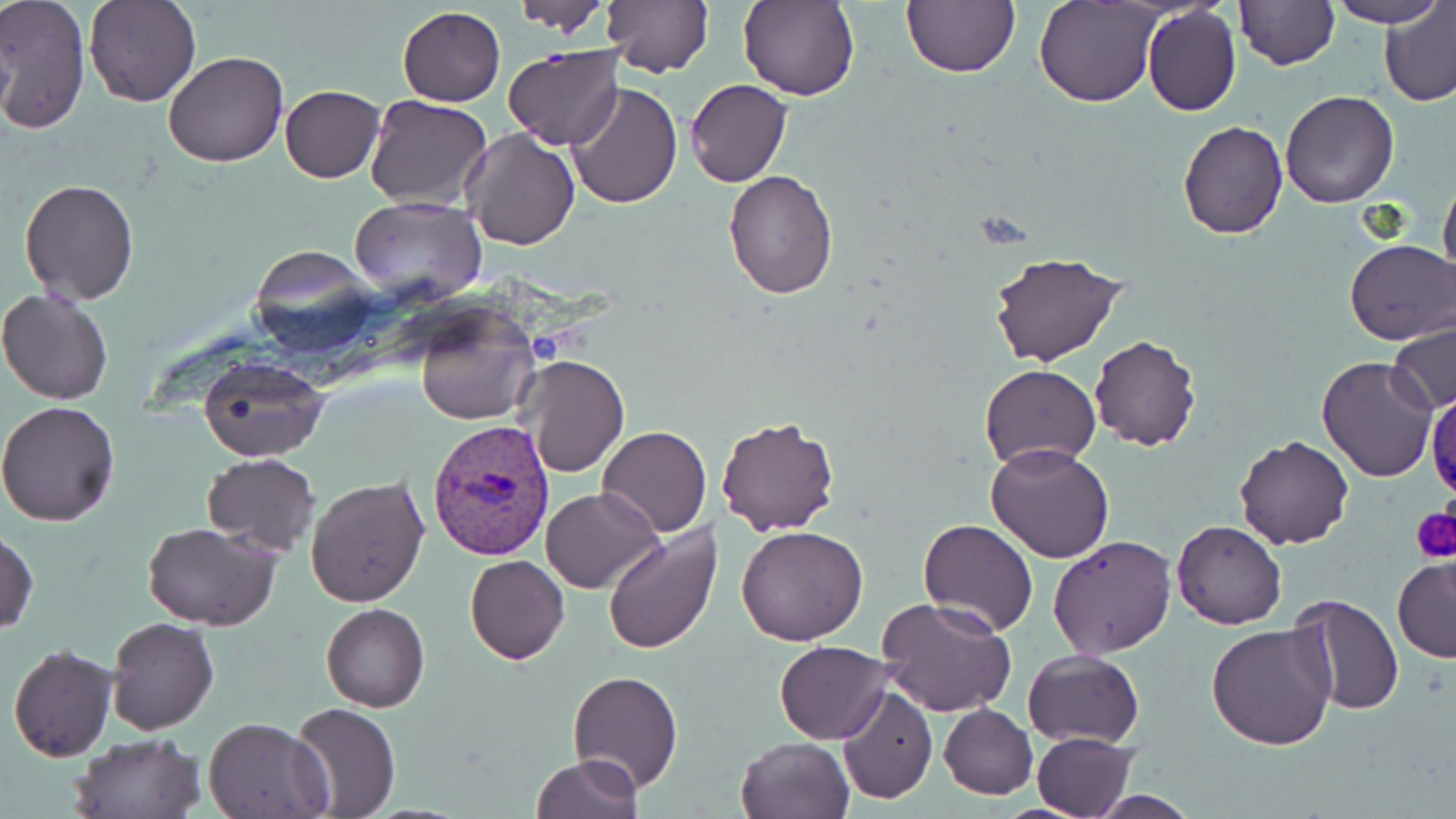
Approximate bounding boxes as named x1/y1/x2/y2 corners in pixels. Uninfected red blood cell locations: (x1=84, y1=0, x2=200, y2=106), (x1=603, y1=0, x2=713, y2=78), (x1=738, y1=0, x2=858, y2=101), (x1=901, y1=0, x2=1019, y2=78), (x1=1035, y1=0, x2=1161, y2=107), (x1=1326, y1=0, x2=1446, y2=26), (x1=1379, y1=0, x2=1456, y2=108), (x1=0, y1=1, x2=90, y2=133), (x1=507, y1=1, x2=609, y2=35), (x1=1233, y1=1, x2=1339, y2=70), (x1=1141, y1=5, x2=1242, y2=117), (x1=397, y1=7, x2=505, y2=105), (x1=504, y1=44, x2=624, y2=151), (x1=163, y1=51, x2=288, y2=167), (x1=685, y1=78, x2=792, y2=187), (x1=568, y1=81, x2=684, y2=211), (x1=279, y1=84, x2=384, y2=182), (x1=1280, y1=90, x2=1399, y2=209), (x1=363, y1=93, x2=492, y2=209), (x1=1177, y1=120, x2=1287, y2=239), (x1=461, y1=127, x2=581, y2=249), (x1=722, y1=169, x2=838, y2=300), (x1=1439, y1=176, x2=1456, y2=289), (x1=19, y1=177, x2=139, y2=303), (x1=348, y1=196, x2=487, y2=307), (x1=1345, y1=239, x2=1455, y2=346), (x1=987, y1=250, x2=1130, y2=369), (x1=0, y1=287, x2=116, y2=404), (x1=411, y1=300, x2=538, y2=425), (x1=1385, y1=318, x2=1454, y2=415), (x1=1088, y1=334, x2=1202, y2=452), (x1=520, y1=355, x2=628, y2=477), (x1=197, y1=356, x2=329, y2=461), (x1=1316, y1=356, x2=1439, y2=482), (x1=980, y1=364, x2=1102, y2=472), (x1=0, y1=400, x2=121, y2=527), (x1=715, y1=416, x2=839, y2=536), (x1=598, y1=425, x2=712, y2=538), (x1=1234, y1=435, x2=1355, y2=550), (x1=984, y1=443, x2=1115, y2=564), (x1=203, y1=453, x2=321, y2=556), (x1=305, y1=474, x2=430, y2=610), (x1=541, y1=487, x2=661, y2=594), (x1=917, y1=518, x2=1040, y2=638), (x1=1171, y1=519, x2=1287, y2=631), (x1=142, y1=521, x2=281, y2=631), (x1=602, y1=523, x2=723, y2=655), (x1=736, y1=525, x2=869, y2=646), (x1=1, y1=529, x2=38, y2=636), (x1=1047, y1=534, x2=1177, y2=658), (x1=465, y1=554, x2=568, y2=665), (x1=1392, y1=554, x2=1456, y2=664), (x1=1286, y1=594, x2=1402, y2=715), (x1=877, y1=597, x2=1017, y2=717), (x1=321, y1=603, x2=429, y2=712), (x1=106, y1=617, x2=219, y2=735), (x1=1205, y1=621, x2=1337, y2=751), (x1=774, y1=641, x2=892, y2=743), (x1=7, y1=643, x2=120, y2=763), (x1=1023, y1=647, x2=1144, y2=746), (x1=567, y1=670, x2=683, y2=792), (x1=835, y1=683, x2=938, y2=805), (x1=289, y1=701, x2=401, y2=817), (x1=939, y1=703, x2=1038, y2=798), (x1=204, y1=717, x2=329, y2=818), (x1=1030, y1=731, x2=1137, y2=819), (x1=68, y1=733, x2=202, y2=818), (x1=735, y1=736, x2=854, y2=819), (x1=531, y1=755, x2=643, y2=819). Platelet locations: (x1=1410, y1=504, x2=1456, y2=560). Plasmodium vivax-infected red blood cell locations: (x1=427, y1=419, x2=557, y2=560). Slide-level diagnosis: Plasmodium vivax. Single field of view. Light microscopy. Image is 1456×819 pixels. May-Grünwald-Giemsa stain. Captured at 1000x magnification. Thin blood smear.